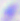

identification = Toxoplasma gondii
magnification = 400x
modality = micrograph